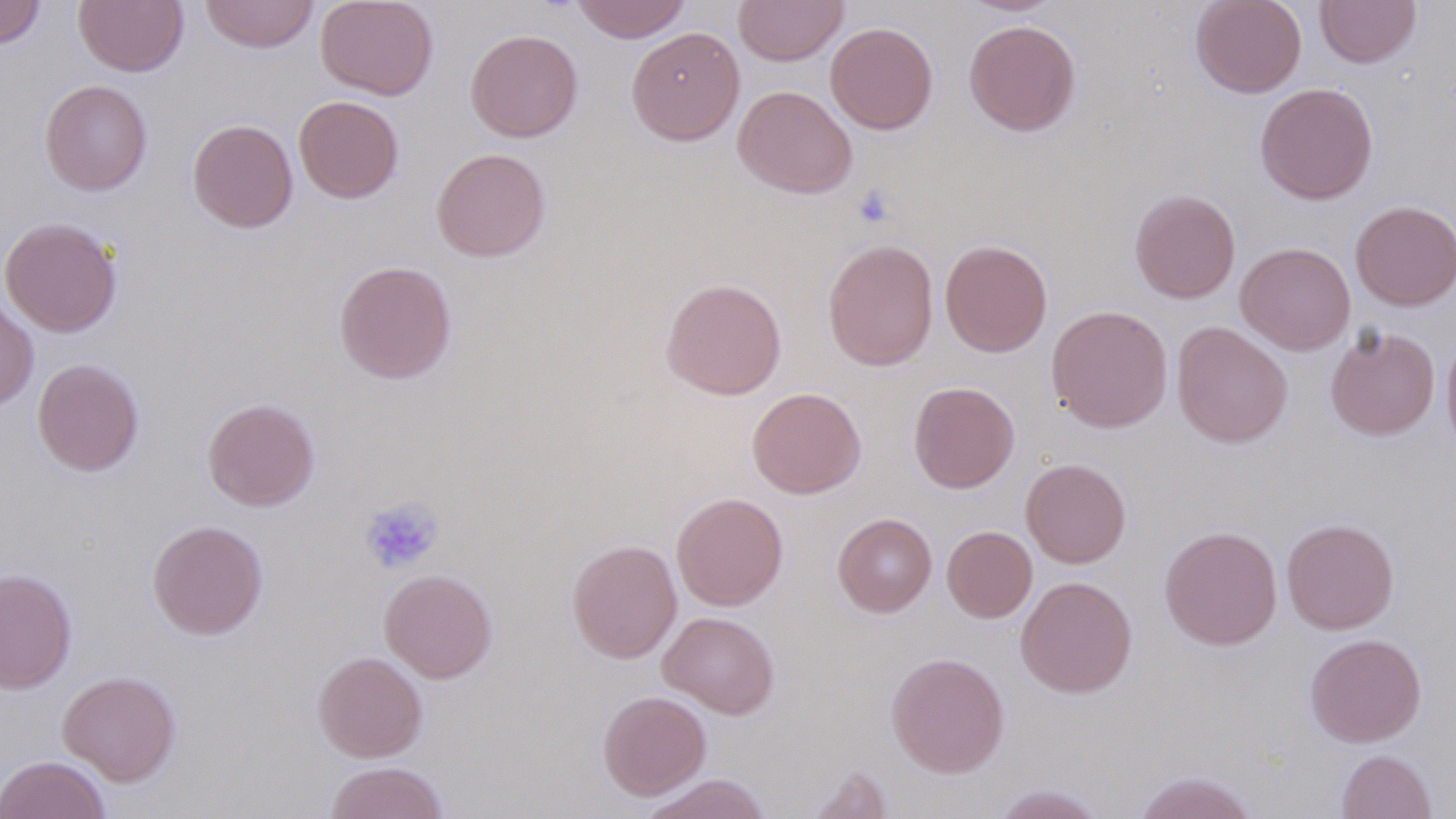

Summary:
  - Coordinate format: approximate bounding boxes as [x1, y1, x2, y2] in pixels
  - Platelet locations: [851, 186, 895, 229], [358, 496, 444, 575]
  - Uninfected red blood cell locations: [0, 0, 46, 49], [74, 0, 189, 77], [200, 0, 320, 53], [315, 0, 439, 101], [570, 0, 691, 43], [733, 0, 849, 66], [961, 0, 1064, 16], [1190, 0, 1307, 97], [1315, 0, 1421, 68], [964, 20, 1081, 136], [825, 22, 938, 135], [626, 27, 745, 146], [465, 29, 583, 142], [39, 79, 153, 195], [1254, 83, 1378, 205], [733, 85, 858, 199], [293, 96, 405, 203], [187, 119, 298, 233], [431, 147, 550, 262], [1129, 188, 1241, 303], [1350, 200, 1456, 310], [0, 216, 123, 337], [823, 238, 939, 371], [939, 240, 1053, 357], [1235, 242, 1355, 355], [333, 260, 457, 385], [660, 278, 787, 399], [0, 295, 38, 410], [1046, 305, 1173, 432], [1171, 322, 1293, 448], [1325, 326, 1440, 440], [1441, 333, 1456, 456], [32, 358, 144, 477], [908, 381, 1020, 493], [747, 387, 866, 499], [202, 397, 320, 511], [1020, 458, 1131, 568], [671, 492, 788, 611], [832, 513, 937, 617], [1281, 518, 1399, 634], [147, 519, 268, 640], [942, 525, 1037, 623], [1159, 525, 1283, 651], [567, 539, 682, 663], [0, 568, 77, 694], [379, 569, 497, 683], [1016, 576, 1138, 698], [659, 611, 780, 719], [1304, 633, 1427, 747], [312, 651, 427, 762], [886, 652, 1009, 778], [57, 670, 182, 786], [597, 690, 711, 801], [1335, 749, 1436, 819], [0, 754, 111, 819], [324, 761, 449, 819], [805, 763, 894, 819], [1131, 770, 1260, 819], [639, 773, 773, 819], [987, 783, 1108, 819]
  - Slide-level diagnosis: negative for blood parasites
  - Field of view: single
  - Preparation: thin blood smear
  - Image size: 1456×819 pixels
  - Stain: May-Grünwald-Giemsa
  - Modality: optical microscopy
  - Magnification: 1000x